Name the blood parasite species.
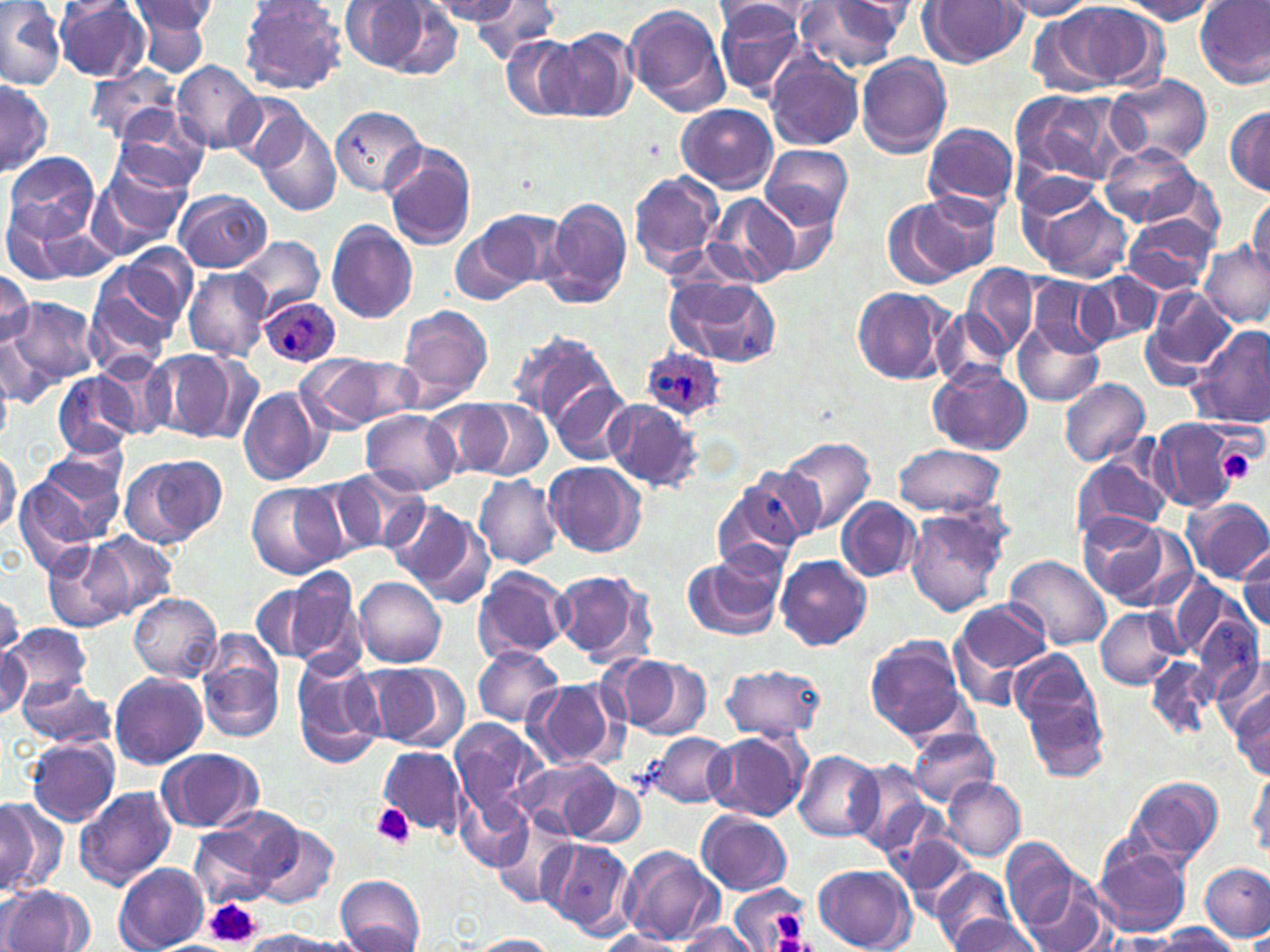

Plasmodium ovale.

Approximate bounding boxes as [x1, y1, x2, y2] in pixels. Platelet locations: [1217, 447, 1258, 485], [372, 803, 416, 848], [207, 899, 260, 949], [774, 910, 804, 939]. Uninfected red blood cell locations: [0, 0, 65, 89], [470, 0, 562, 64], [918, 0, 1026, 66], [126, 1, 217, 71], [238, 1, 348, 95], [426, 1, 524, 24], [997, 1, 1098, 20], [1116, 1, 1218, 24], [1196, 1, 1269, 88], [337, 2, 454, 81], [715, 2, 816, 46], [795, 2, 907, 75], [53, 3, 153, 81], [623, 3, 729, 117], [712, 3, 810, 97], [1033, 4, 1155, 93], [550, 28, 639, 123], [502, 38, 583, 121], [856, 54, 953, 158], [766, 55, 865, 151], [171, 60, 263, 152], [87, 68, 185, 146], [1108, 73, 1213, 165], [0, 76, 52, 177], [1009, 89, 1118, 188], [228, 91, 314, 175], [678, 103, 777, 194], [328, 105, 425, 198], [1224, 105, 1270, 194], [110, 110, 211, 196], [253, 112, 342, 216], [922, 123, 1019, 213], [382, 143, 476, 251], [1098, 144, 1206, 231], [760, 145, 854, 229], [3, 152, 100, 245], [91, 159, 192, 254], [629, 171, 724, 274], [172, 189, 272, 271], [1025, 189, 1133, 284], [913, 191, 1004, 277], [758, 193, 841, 276], [1247, 193, 1270, 280], [704, 194, 801, 288], [542, 198, 632, 310], [883, 200, 972, 290], [0, 203, 100, 286], [1122, 214, 1215, 295], [326, 220, 419, 326], [449, 220, 541, 308], [232, 235, 324, 317], [1201, 243, 1269, 326], [113, 246, 200, 334], [962, 262, 1040, 357], [84, 266, 182, 371], [183, 268, 273, 360], [0, 269, 33, 352], [1077, 271, 1163, 348], [664, 274, 782, 369], [1028, 276, 1112, 357], [1142, 285, 1239, 385], [851, 286, 958, 386], [5, 297, 97, 395], [394, 304, 496, 411], [935, 306, 1014, 391], [1011, 318, 1104, 408], [1186, 325, 1270, 429], [513, 330, 621, 432], [1, 332, 47, 413], [143, 349, 242, 441], [294, 352, 417, 433], [928, 363, 1031, 456], [543, 370, 633, 467], [53, 372, 136, 459], [1058, 378, 1151, 467], [238, 385, 333, 487], [425, 397, 525, 477], [465, 400, 552, 481], [603, 400, 704, 492], [360, 409, 461, 496], [1149, 417, 1244, 513], [777, 436, 877, 534], [891, 444, 1009, 518], [36, 445, 128, 523], [0, 449, 20, 536], [121, 452, 227, 547], [1073, 456, 1170, 544], [16, 459, 122, 562], [544, 462, 646, 557], [314, 468, 422, 559], [711, 473, 815, 573], [474, 474, 563, 568], [246, 482, 344, 578], [836, 497, 922, 582], [1183, 497, 1270, 584], [392, 502, 497, 608], [903, 508, 1010, 618], [1077, 516, 1180, 609], [87, 531, 179, 618], [43, 540, 135, 632], [1237, 545, 1269, 635], [681, 552, 786, 642], [775, 554, 871, 651], [1003, 555, 1111, 651], [281, 566, 369, 674], [472, 567, 572, 663], [550, 567, 656, 665], [353, 576, 447, 669], [251, 581, 335, 665], [0, 590, 25, 657], [128, 593, 221, 681], [951, 599, 1053, 701], [1095, 607, 1180, 689], [0, 624, 90, 706], [864, 635, 967, 740], [197, 636, 285, 742], [472, 645, 563, 727], [0, 647, 31, 718], [1013, 654, 1108, 779], [290, 655, 388, 769], [1146, 656, 1215, 738], [611, 657, 713, 736], [1218, 660, 1270, 743], [358, 661, 468, 752], [717, 663, 826, 740], [109, 671, 208, 769], [15, 674, 118, 748], [525, 680, 621, 771], [1230, 689, 1270, 781], [448, 718, 547, 825], [907, 725, 999, 806], [645, 730, 734, 810], [706, 730, 811, 822], [26, 738, 122, 826], [376, 746, 468, 835], [157, 747, 264, 834], [793, 751, 884, 841], [515, 758, 623, 837], [845, 758, 932, 853], [1248, 766, 1269, 859], [561, 772, 647, 850], [1125, 775, 1225, 868], [942, 776, 1026, 860], [73, 787, 177, 890], [0, 795, 67, 898], [458, 795, 533, 872], [492, 809, 577, 908], [695, 810, 793, 896], [186, 817, 290, 910], [248, 823, 339, 910], [888, 830, 981, 916], [1092, 834, 1194, 938], [1002, 837, 1083, 935], [539, 839, 634, 936], [621, 847, 724, 947], [1013, 861, 1109, 952], [1200, 861, 1270, 943], [113, 864, 208, 951], [812, 864, 914, 952], [932, 868, 1016, 951], [333, 874, 426, 952], [0, 885, 94, 952], [727, 885, 811, 952], [944, 915, 1044, 952], [671, 922, 758, 952], [1155, 923, 1239, 951], [596, 928, 686, 951], [238, 930, 351, 951], [469, 934, 560, 951]. Plasmodium ovale-infected red blood cell locations: [260, 294, 341, 367], [636, 348, 727, 426]. Captured at 1000x magnification. Thin blood film. May-Grünwald-Giemsa stain. One field of a larger specimen. Light microscopy. Image is 1270×952 pixels.